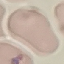
Result: no malaria parasites seen. Photographed with a smartphone camera at the microscope eyepiece. Automatically extracted cell patch, resized to 64 × 64 pixels. Thin blood smear. Giemsa stain.